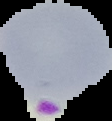

preparation = thin blood smear
result = malaria parasites detected
image type = cell region segmented out of the field of view; surrounding area masked to black
image size = 112×121 pixels